Name the blood parasite species.
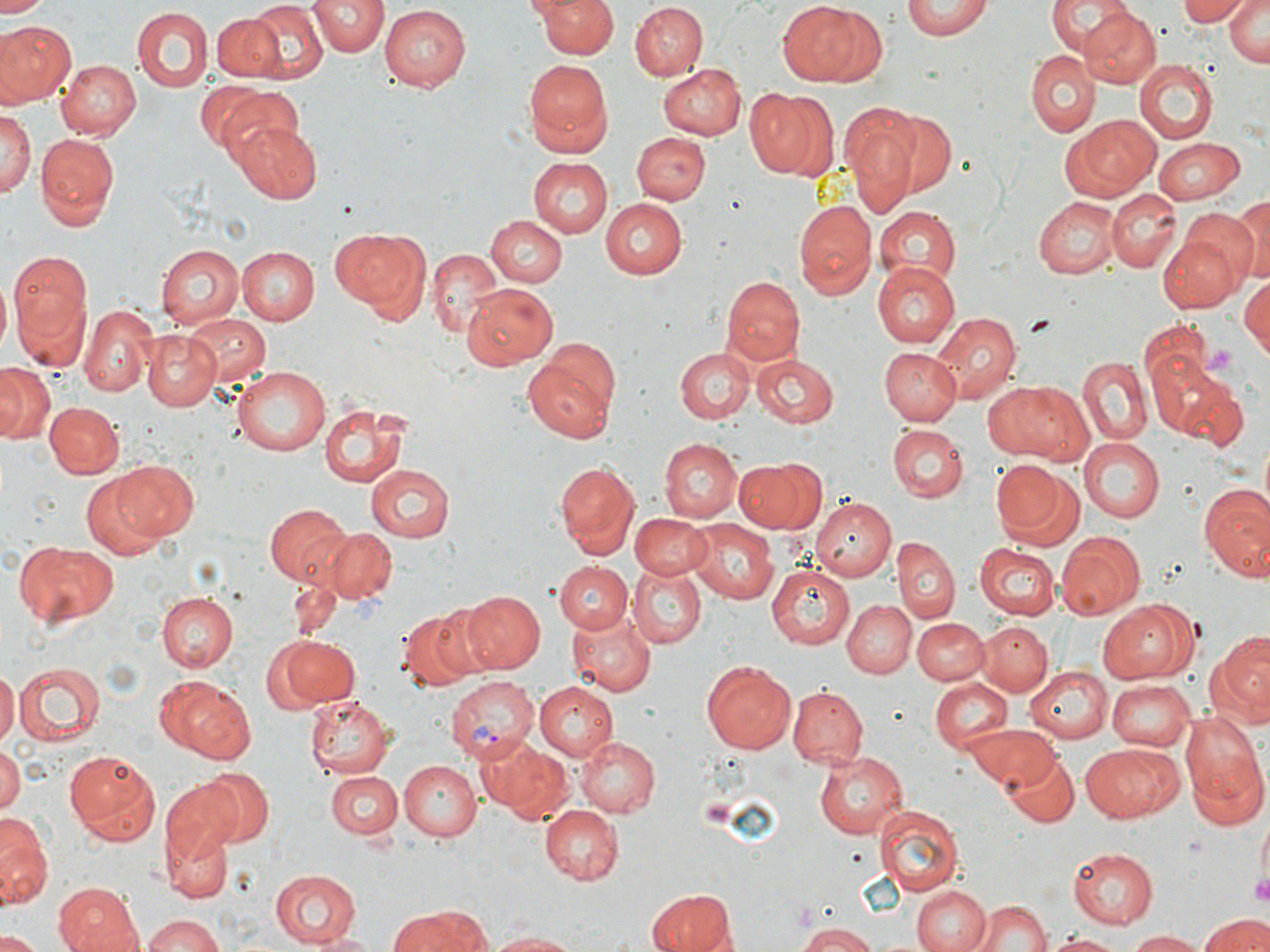
Plasmodium vivax.

Approximate bounding boxes as named x1/y1/x2/y2 corners in pixels. Plasmodium vivax-infected red blood cell locations: (x1=446, y1=677, x2=540, y2=761). Platelet locations: (x1=1201, y1=347, x2=1238, y2=378), (x1=1254, y1=867, x2=1270, y2=908). Uninfected red blood cell locations: (x1=310, y1=0, x2=386, y2=57), (x1=533, y1=0, x2=619, y2=59), (x1=902, y1=0, x2=992, y2=40), (x1=1046, y1=0, x2=1130, y2=55), (x1=1178, y1=0, x2=1249, y2=26), (x1=777, y1=1, x2=879, y2=88), (x1=2, y1=2, x2=50, y2=18), (x1=246, y1=2, x2=326, y2=80), (x1=1224, y1=2, x2=1268, y2=67), (x1=631, y1=3, x2=708, y2=82), (x1=378, y1=4, x2=467, y2=89), (x1=1076, y1=5, x2=1160, y2=88), (x1=132, y1=8, x2=212, y2=91), (x1=212, y1=10, x2=285, y2=82), (x1=1, y1=20, x2=75, y2=103), (x1=1024, y1=50, x2=1100, y2=137), (x1=57, y1=59, x2=141, y2=139), (x1=521, y1=59, x2=613, y2=155), (x1=1133, y1=60, x2=1216, y2=144), (x1=657, y1=63, x2=747, y2=139), (x1=203, y1=84, x2=293, y2=161), (x1=747, y1=86, x2=838, y2=182), (x1=860, y1=103, x2=957, y2=200), (x1=0, y1=107, x2=34, y2=207), (x1=842, y1=110, x2=921, y2=216), (x1=1063, y1=114, x2=1161, y2=202), (x1=230, y1=120, x2=322, y2=204), (x1=624, y1=126, x2=705, y2=268), (x1=634, y1=131, x2=710, y2=205), (x1=34, y1=134, x2=118, y2=230), (x1=1152, y1=138, x2=1246, y2=202), (x1=529, y1=155, x2=614, y2=237), (x1=1107, y1=189, x2=1181, y2=271), (x1=1034, y1=197, x2=1119, y2=279), (x1=598, y1=198, x2=687, y2=279), (x1=1229, y1=198, x2=1270, y2=282), (x1=794, y1=199, x2=876, y2=299), (x1=874, y1=206, x2=961, y2=285), (x1=1179, y1=210, x2=1259, y2=289), (x1=486, y1=216, x2=567, y2=288), (x1=330, y1=228, x2=425, y2=311), (x1=1158, y1=232, x2=1243, y2=312), (x1=156, y1=245, x2=244, y2=330), (x1=235, y1=245, x2=320, y2=326), (x1=427, y1=249, x2=504, y2=339), (x1=10, y1=251, x2=93, y2=370), (x1=872, y1=262, x2=959, y2=349), (x1=1239, y1=273, x2=1270, y2=360), (x1=721, y1=277, x2=805, y2=363), (x1=464, y1=283, x2=557, y2=369), (x1=80, y1=303, x2=156, y2=396), (x1=932, y1=312, x2=1020, y2=404), (x1=184, y1=314, x2=271, y2=394), (x1=142, y1=330, x2=222, y2=411), (x1=522, y1=343, x2=621, y2=445), (x1=882, y1=345, x2=962, y2=424), (x1=675, y1=348, x2=754, y2=423), (x1=1148, y1=353, x2=1246, y2=447), (x1=750, y1=355, x2=838, y2=427), (x1=1079, y1=359, x2=1151, y2=444), (x1=0, y1=363, x2=53, y2=444), (x1=231, y1=367, x2=331, y2=456), (x1=987, y1=380, x2=1091, y2=464), (x1=45, y1=402, x2=122, y2=478), (x1=317, y1=403, x2=412, y2=489), (x1=888, y1=425, x2=967, y2=503), (x1=1257, y1=436, x2=1270, y2=515), (x1=659, y1=438, x2=742, y2=523), (x1=1078, y1=439, x2=1163, y2=524), (x1=112, y1=458, x2=199, y2=541), (x1=736, y1=458, x2=825, y2=533), (x1=991, y1=459, x2=1075, y2=543), (x1=553, y1=461, x2=638, y2=555), (x1=362, y1=464, x2=454, y2=542), (x1=81, y1=473, x2=172, y2=561), (x1=1197, y1=483, x2=1270, y2=581), (x1=810, y1=498, x2=894, y2=583), (x1=263, y1=502, x2=352, y2=585), (x1=631, y1=512, x2=708, y2=578), (x1=686, y1=518, x2=776, y2=604), (x1=323, y1=528, x2=396, y2=604), (x1=1056, y1=530, x2=1146, y2=618), (x1=894, y1=538, x2=958, y2=624), (x1=16, y1=542, x2=118, y2=627), (x1=974, y1=542, x2=1058, y2=618), (x1=553, y1=561, x2=634, y2=632), (x1=767, y1=563, x2=854, y2=649), (x1=629, y1=564, x2=706, y2=648), (x1=459, y1=589, x2=544, y2=674), (x1=156, y1=592, x2=237, y2=672), (x1=842, y1=598, x2=916, y2=678), (x1=1100, y1=599, x2=1194, y2=684), (x1=399, y1=605, x2=489, y2=689), (x1=567, y1=613, x2=655, y2=697), (x1=912, y1=617, x2=988, y2=685), (x1=976, y1=621, x2=1052, y2=696), (x1=1207, y1=634, x2=1270, y2=729), (x1=271, y1=636, x2=358, y2=707), (x1=701, y1=659, x2=797, y2=753), (x1=16, y1=663, x2=105, y2=744), (x1=1026, y1=665, x2=1112, y2=741), (x1=0, y1=670, x2=18, y2=748), (x1=153, y1=673, x2=255, y2=765), (x1=930, y1=677, x2=1012, y2=753), (x1=1108, y1=679, x2=1196, y2=750), (x1=533, y1=682, x2=618, y2=760), (x1=787, y1=686, x2=868, y2=767), (x1=303, y1=695, x2=390, y2=778), (x1=1179, y1=715, x2=1270, y2=829), (x1=967, y1=724, x2=1059, y2=789), (x1=479, y1=737, x2=574, y2=825), (x1=578, y1=737, x2=659, y2=817), (x1=1082, y1=741, x2=1183, y2=821), (x1=0, y1=747, x2=23, y2=814), (x1=64, y1=750, x2=161, y2=845), (x1=1001, y1=750, x2=1079, y2=828), (x1=813, y1=751, x2=908, y2=837), (x1=397, y1=760, x2=480, y2=839), (x1=198, y1=766, x2=273, y2=845), (x1=325, y1=769, x2=403, y2=841), (x1=160, y1=781, x2=243, y2=864), (x1=873, y1=802, x2=964, y2=897), (x1=539, y1=805, x2=621, y2=885), (x1=1258, y1=815, x2=1270, y2=893), (x1=0, y1=820, x2=51, y2=909), (x1=164, y1=827, x2=230, y2=903), (x1=1065, y1=847, x2=1159, y2=931), (x1=268, y1=868, x2=361, y2=947), (x1=911, y1=882, x2=992, y2=952), (x1=54, y1=883, x2=144, y2=952), (x1=646, y1=891, x2=736, y2=952), (x1=974, y1=897, x2=1051, y2=952), (x1=389, y1=907, x2=490, y2=952), (x1=140, y1=913, x2=229, y2=952), (x1=1198, y1=913, x2=1270, y2=952), (x1=794, y1=922, x2=880, y2=952), (x1=1125, y1=930, x2=1211, y2=951), (x1=485, y1=931, x2=584, y2=951), (x1=0, y1=932, x2=44, y2=952), (x1=305, y1=932, x2=383, y2=951), (x1=1045, y1=932, x2=1125, y2=951). One field of a larger specimen. May-Grünwald-Giemsa stain. Light microscopy. Image is 1270×952 pixels. Captured at 1000x magnification. Thin blood smear.